Look for Plasmodium parasites.
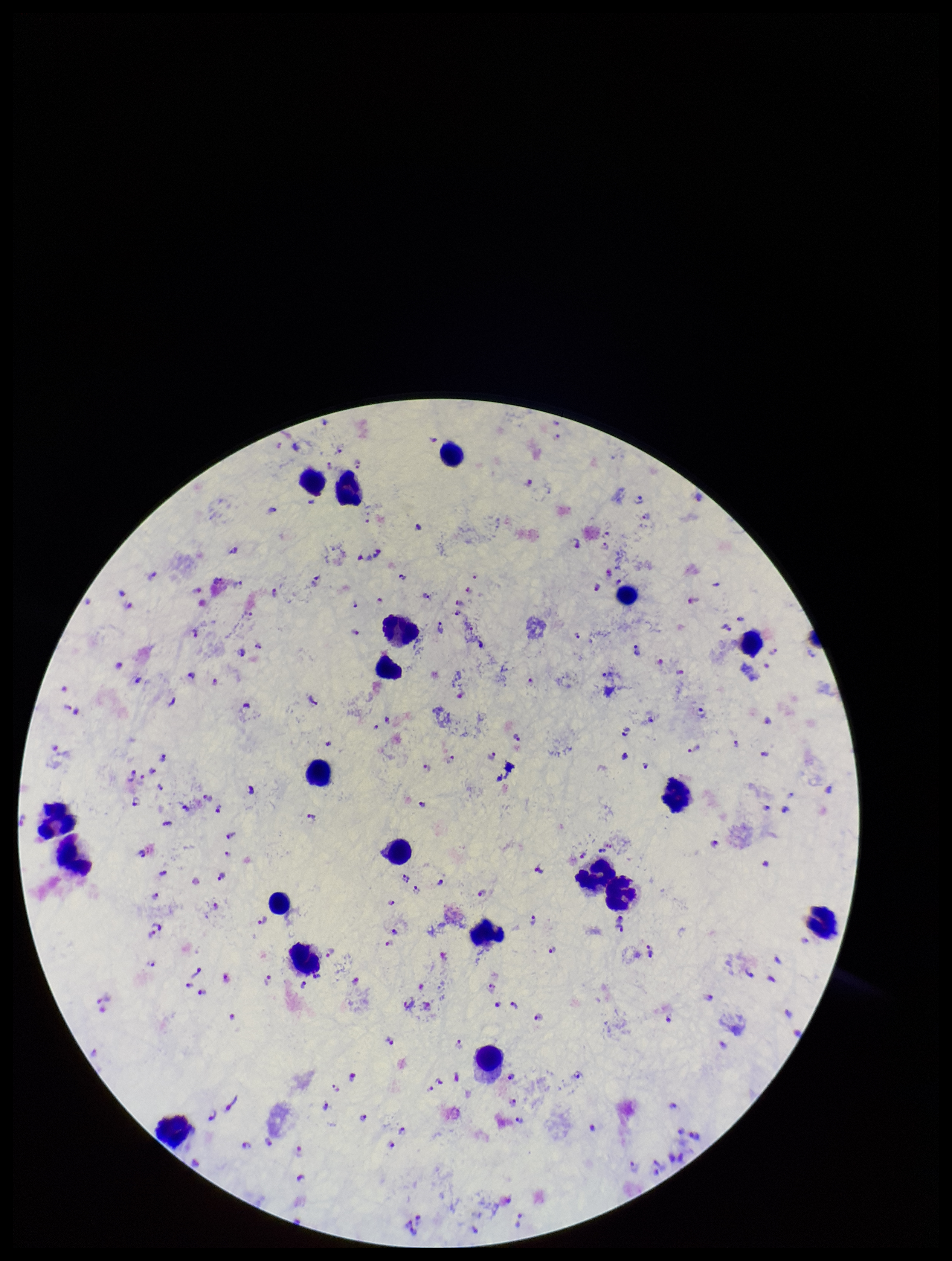

Detected.

Leukocyte count: 21. Smartphone photograph taken through the eyepiece of a microscope. Image is 952×1261 pixels. Preparation: thick blood smear. Giemsa stain. Patient malaria status: positive. Species reported for this patient: Plasmodium falciparum. Parasite count: 198. One field from this slide.